Locate every Plasmodium parasite.
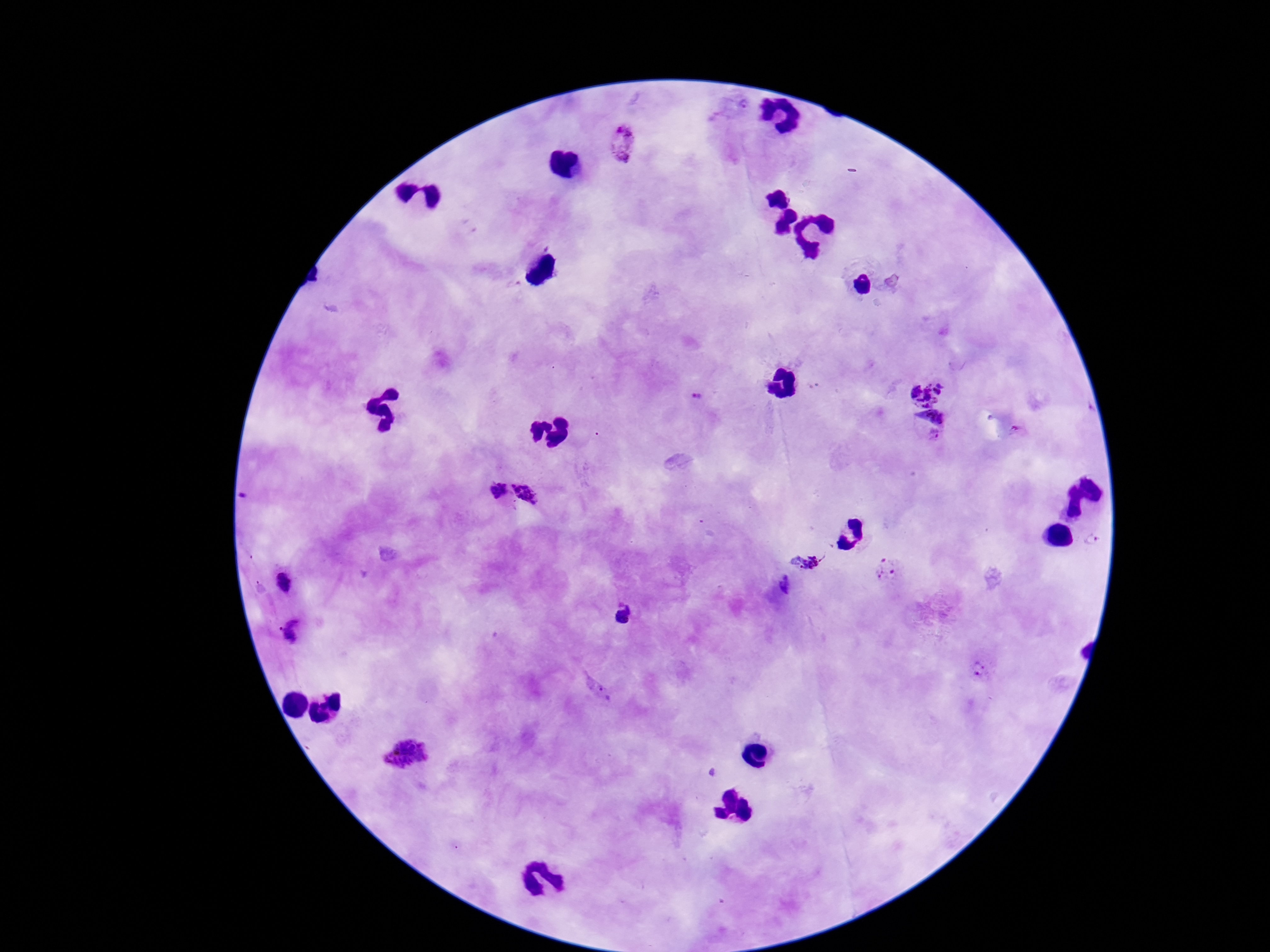

Approximate object centers, in pixels from the top-left corner.
Plasmodium parasites: (x=624, y=145), (x=926, y=388), (x=698, y=394), (x=933, y=413), (x=1016, y=431), (x=934, y=437), (x=497, y=489), (x=525, y=497), (x=1090, y=541), (x=805, y=562), (x=884, y=570), (x=282, y=579), (x=622, y=615), (x=293, y=633), (x=979, y=669), (x=407, y=756).

field_of_view: one from this slide
stain: Giemsa
capture: smartphone camera through the microscope eyepiece
image_size: 1270×952 pixels
magnification: 100x
preparation: thick blood film
patient_malaria_status: positive